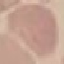

Summary:
  - Malaria status: uninfected
  - Preparation: thin blood smear
  - Stain: Giemsa
  - Capture: smartphone through the microscope eyepiece
  - Image type: cell patch, automatically extracted from a larger field of view and resized to 64 × 64 pixels